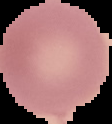

Summary:
  - Image size: 112×124 pixels
  - Image type: segmented cell region on a black background
  - Preparation: thin blood smear
  - Result: no Plasmodium parasites detected